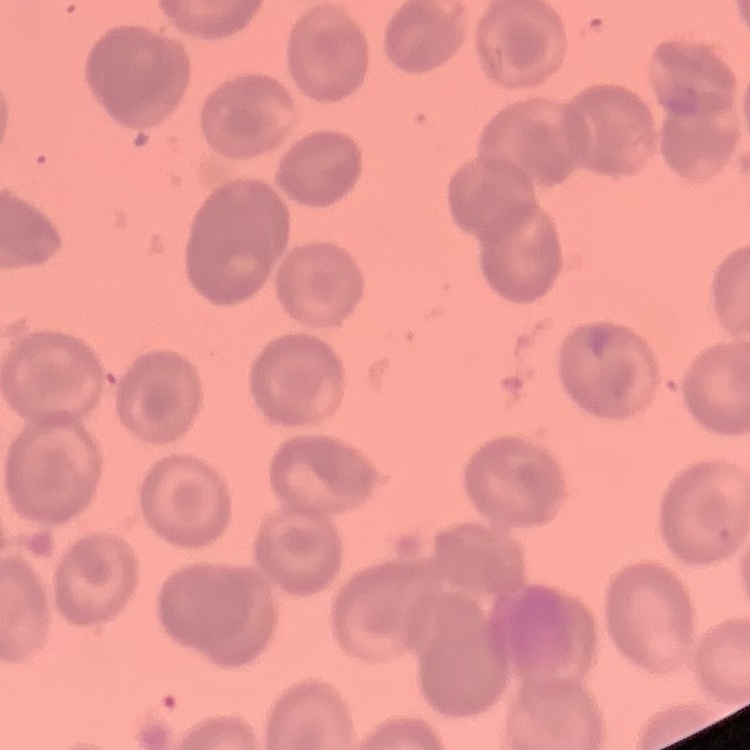

{
  "erythrocyte_morphology": "no rouleaux formation",
  "image_type": "one tile cut from a larger photomicrograph",
  "preparation": "thin peripheral smear",
  "stain": "Field's or Giemsa"
}